Give the extent of all uninfected red blood cells.
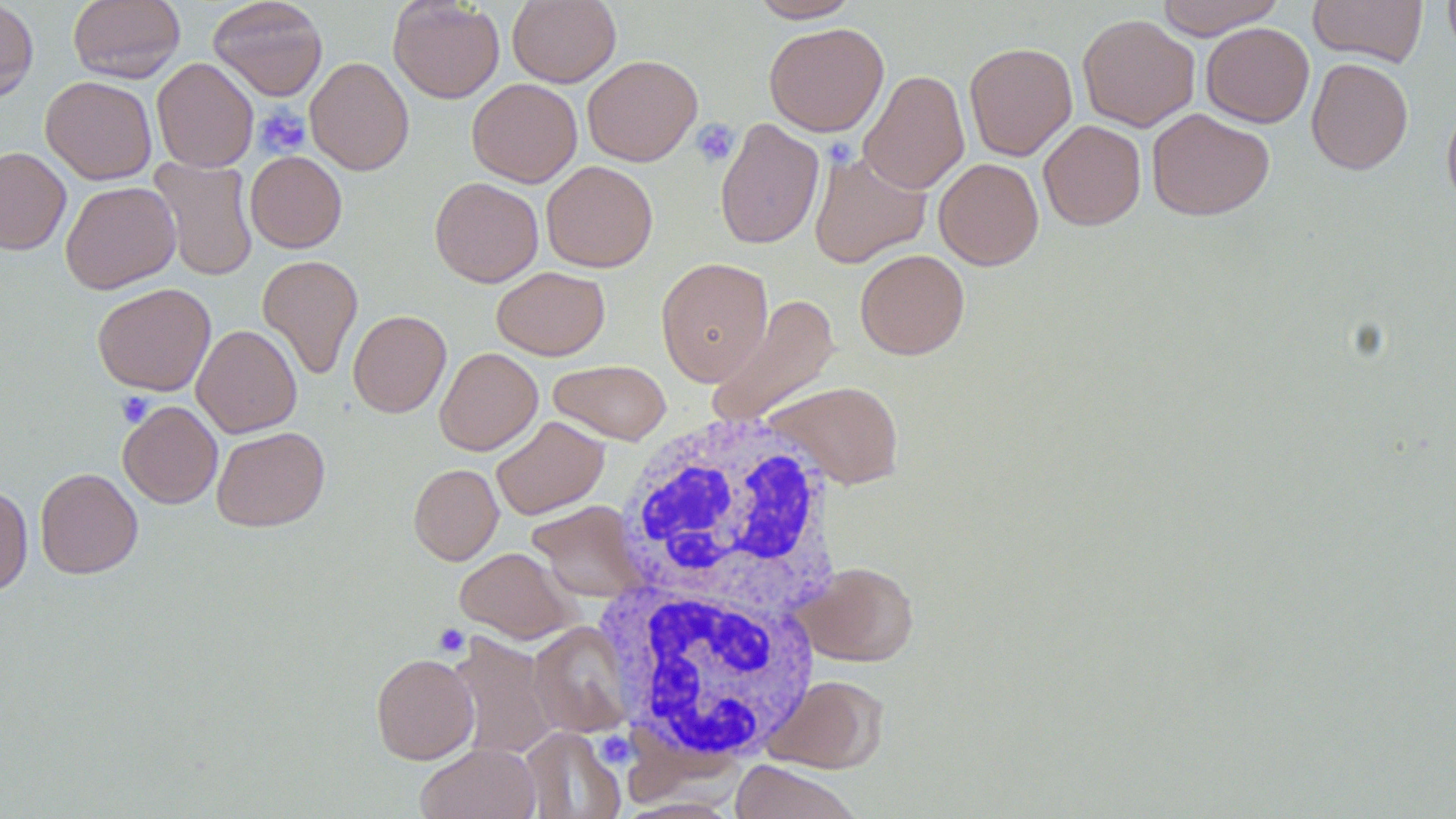

Approximate bounding boxes as [x1, y1, x2, y2] in pixels.
Uninfected red blood cells: [0, 0, 38, 104], [67, 0, 186, 84], [208, 0, 328, 100], [388, 0, 505, 103], [507, 0, 621, 88], [749, 0, 862, 22], [1154, 0, 1285, 38], [1308, 0, 1428, 67], [1442, 0, 1456, 63], [1077, 13, 1200, 132], [763, 22, 889, 136], [1201, 22, 1314, 128], [963, 42, 1077, 161], [582, 54, 703, 166], [152, 57, 258, 172], [305, 57, 414, 175], [1307, 58, 1414, 175], [858, 69, 970, 195], [41, 76, 157, 185], [467, 78, 582, 187], [1441, 97, 1456, 212], [1146, 107, 1274, 220], [715, 118, 825, 250], [1038, 120, 1146, 230], [0, 147, 71, 255], [809, 148, 931, 268], [245, 151, 347, 253], [149, 157, 258, 281], [933, 158, 1044, 270], [541, 161, 658, 272], [430, 177, 544, 287], [60, 181, 181, 294], [855, 249, 970, 360], [257, 255, 363, 380], [656, 257, 773, 386], [492, 266, 610, 360], [92, 283, 216, 395], [705, 294, 841, 429], [348, 309, 451, 417], [191, 324, 302, 438], [434, 347, 543, 456], [548, 359, 671, 445], [762, 380, 906, 489], [118, 401, 222, 508], [491, 415, 610, 520], [211, 426, 330, 532], [408, 463, 504, 565], [35, 467, 143, 579], [0, 485, 33, 597], [527, 500, 646, 602], [454, 547, 578, 643], [800, 561, 919, 666], [529, 622, 633, 737], [448, 633, 559, 760], [370, 652, 479, 764], [764, 674, 889, 773], [519, 727, 626, 819], [415, 743, 541, 819], [729, 760, 864, 819].

Platelet locations: [254, 104, 311, 158], [691, 118, 739, 167], [829, 141, 851, 161], [116, 392, 155, 427], [432, 624, 470, 657], [603, 739, 630, 766]. White blood cell locations: [611, 412, 844, 621], [600, 579, 822, 765]. Slide-level diagnosis: negative for blood parasites. Captured at 1000x magnification. May-Grünwald-Giemsa-stained preparation. Thin blood smear. Image is 1456×819 pixels. One field of a larger specimen. Light microscopy.